Comment on the morphology of the red blood cells.
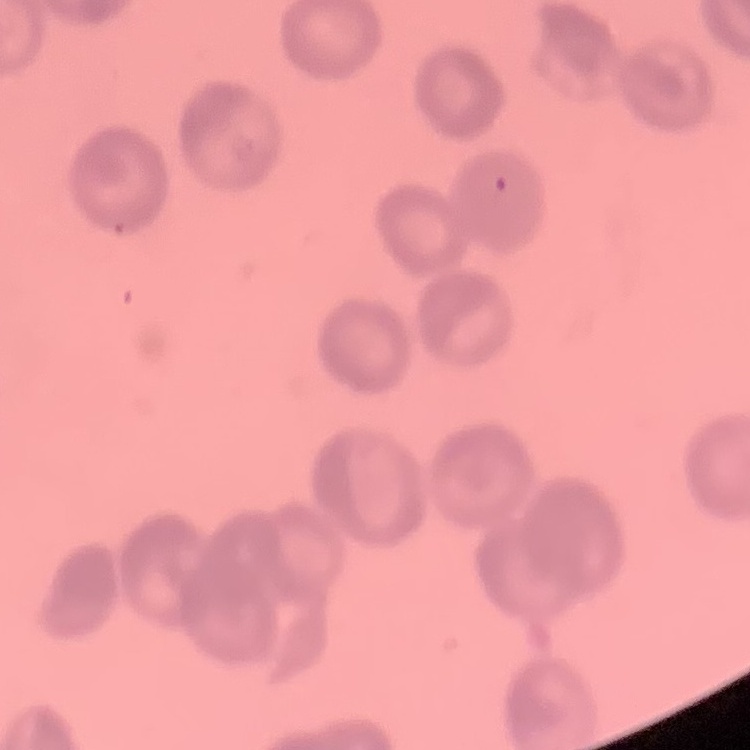
They show rouleaux formation.

One tile cut from a larger photomicrograph. Stained with either Field's or Giemsa. Thin blood film.